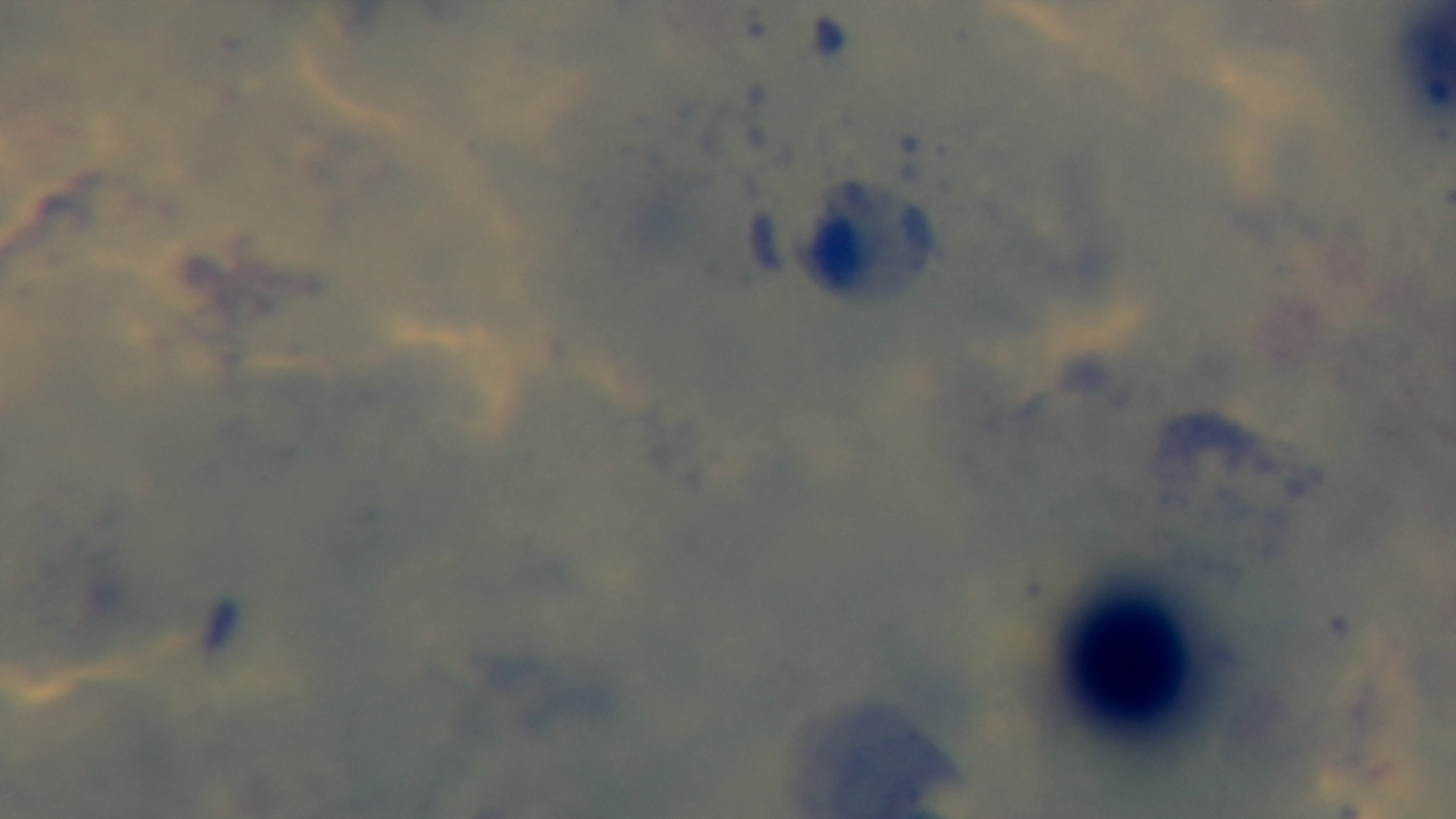 Giemsa-stained. Malaria status: uninfected. 100x oil-immersion objective. Captured with a mounted 4K digital camera. Photomicrograph. One field from the slide. Preparation: thick smear.